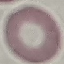
Result: negative for malaria parasites. Thin smear of blood. Automatically extracted cell patch, resized to 64 × 64 pixels. Giemsa-stained preparation. Photographed with a smartphone camera at the microscope eyepiece.